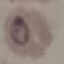
Malaria status: parasitized. Thin smear of blood. Acquired by smartphone through the microscope eyepiece. Giemsa stain. Automatically extracted cell patch, resized to 64 × 64 pixels.